Report the malaria status of this cell.
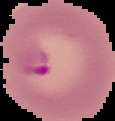
It is parasitized.

image type = segmented cell region on a black background
preparation = thin blood smear
image size = 115×121 pixels